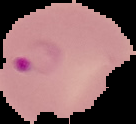

preparation: thin blood film
image_size: 136×124 pixels
image_type: cell region segmented out of the field of view; surrounding area masked to black
result: malaria parasites detected